Give a bounding box for every Plasmodium parasite.
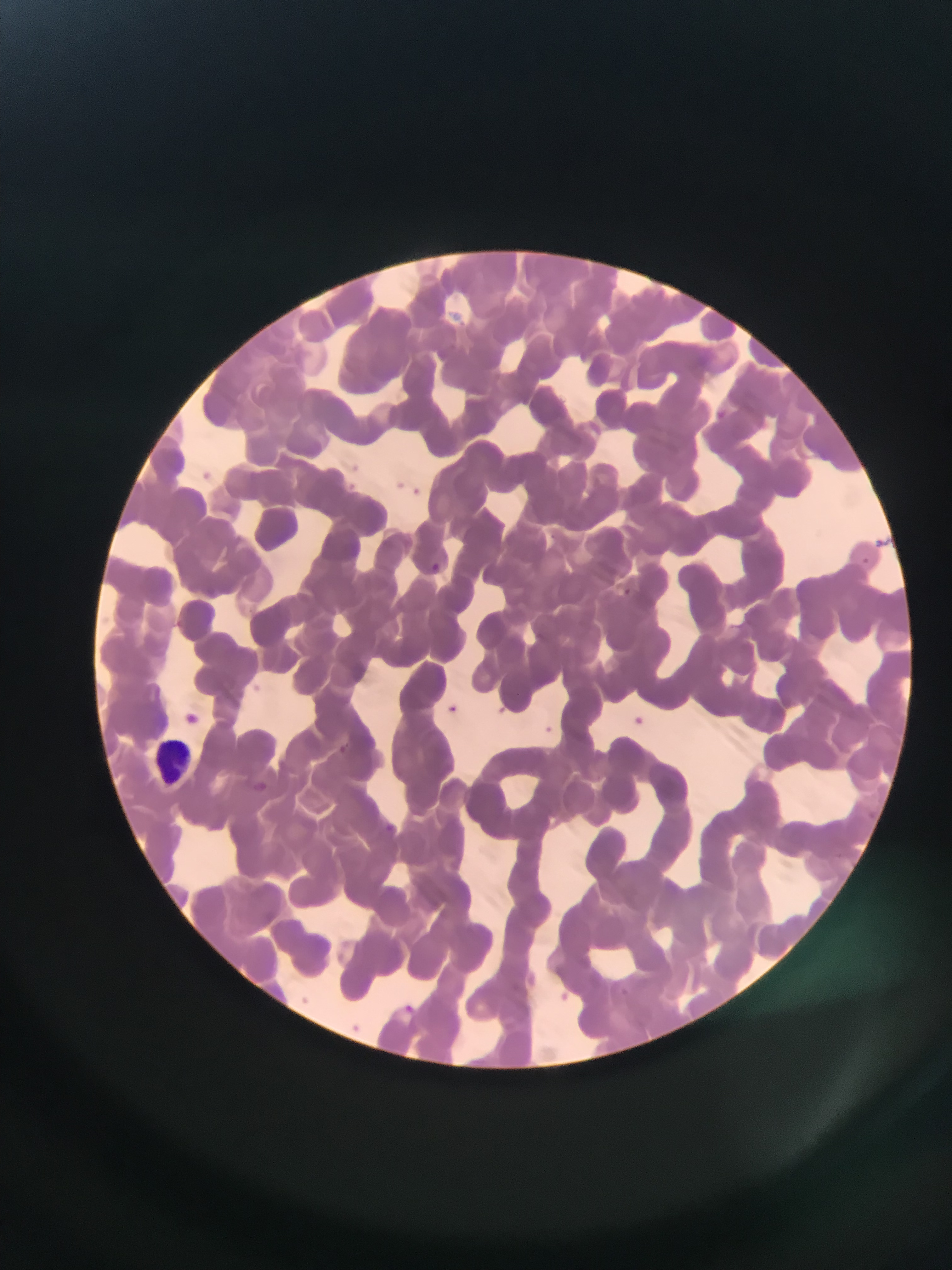
Approximate bounding boxes as {left, top, right, bottom} in pixels.
Plasmodium parasites: {714, 408, 729, 423}, {546, 528, 561, 541}, {432, 556, 443, 568}, {620, 587, 633, 598}, {446, 705, 460, 718}, {625, 712, 649, 733}, {539, 721, 558, 739}, {333, 745, 354, 755}, {380, 819, 397, 834}, {397, 1000, 419, 1018}.

Leukocyte locations: {154, 733, 202, 784}. Image is 952×1270 pixels. Sample from Ghana. Mobile-phone photograph taken through the microscope. Thin blood smear. One field of view.